Assess this cell for malaria.
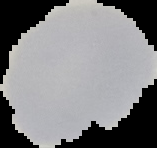

Uninfected.

{
  "image_size": "157×148 pixels",
  "image_type": "segmented cell region with the area outside set to black",
  "preparation": "thin blood smear"
}